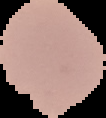

preparation = thin blood film
result = no Plasmodium parasites seen
image type = segmented cell region on a black background
image size = 106×118 pixels